Classify this cell by malaria status.
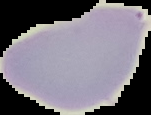
It is uninfected.

Image is 151×115 pixels. From a thin blood smear. Segmented cell region on a black background.